Report the malaria status of this cell.
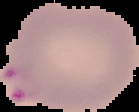

Parasitized.

{
  "preparation": "thin blood film",
  "image_size": "139×112 pixels",
  "image_type": "segmented cell region on a black background"
}